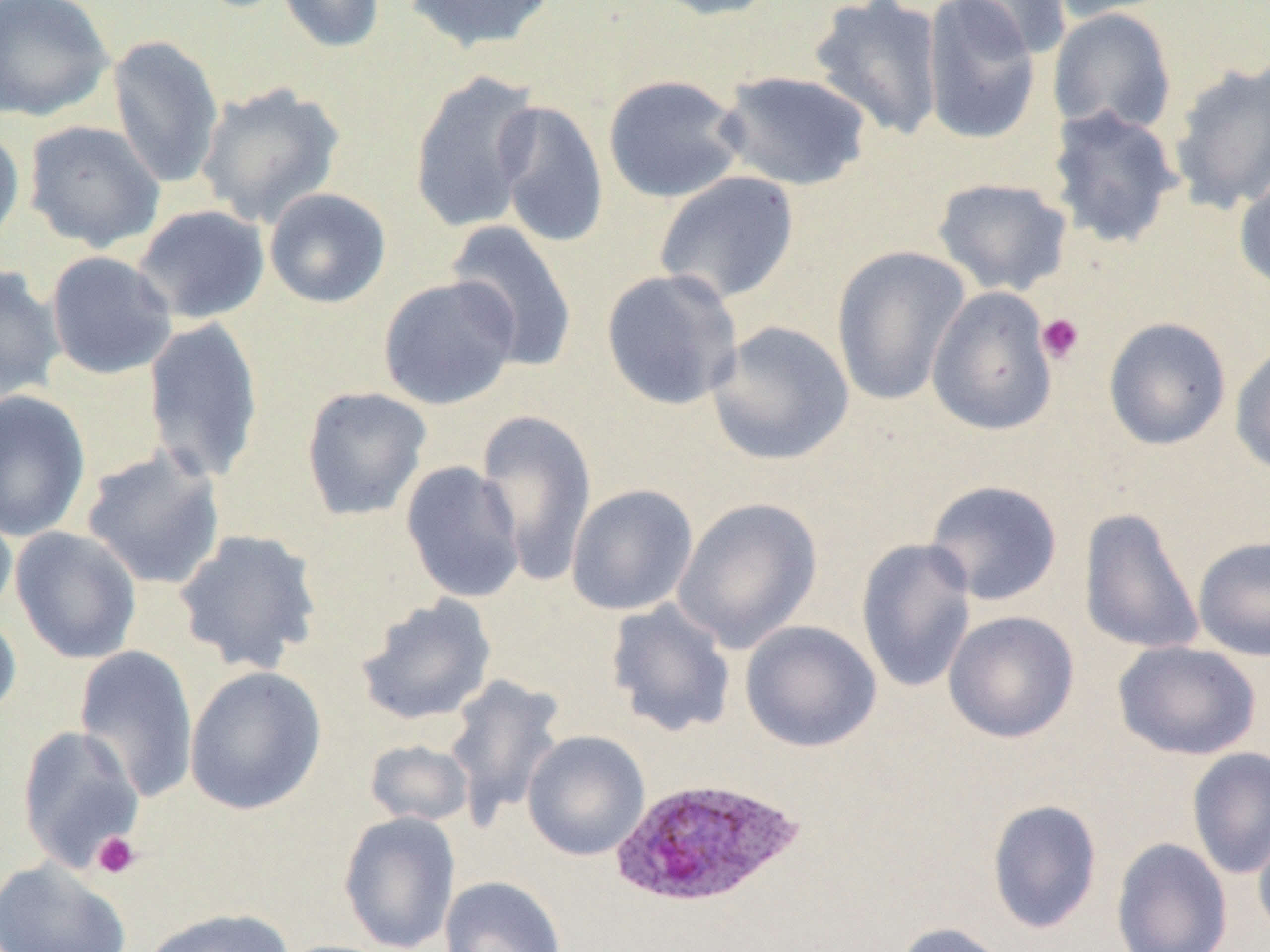

slide-level diagnosis = Plasmodium ovale
image size = 1270×952 pixels
preparation = thin blood film
modality = optical microscopy
field of view = one of a larger specimen
magnification = 1000x
uninfected red blood cell locations = approximate bounding boxes as [x1, y1, x2, y2] in pixels: [0, 0, 114, 122], [275, 0, 385, 54], [403, 0, 559, 52], [645, 0, 785, 21], [807, 0, 946, 141], [920, 0, 1043, 146], [946, 0, 1071, 60], [1041, 0, 1177, 23], [1047, 8, 1177, 137], [106, 34, 225, 190], [1167, 59, 1270, 217], [408, 70, 544, 233], [715, 70, 874, 192], [601, 74, 747, 204], [195, 82, 346, 228], [492, 100, 610, 250], [1045, 105, 1184, 249], [23, 120, 166, 252], [0, 126, 25, 254], [1234, 163, 1270, 294], [653, 171, 801, 307], [931, 177, 1074, 297], [264, 188, 392, 309], [132, 204, 270, 325], [445, 220, 579, 372], [831, 245, 972, 406], [45, 251, 178, 380], [0, 264, 64, 404], [600, 268, 744, 411], [378, 275, 521, 410], [926, 286, 1059, 437], [142, 317, 264, 484], [1103, 317, 1232, 451], [707, 320, 855, 466], [1230, 339, 1270, 477], [300, 386, 433, 521], [0, 389, 92, 542], [476, 409, 598, 586], [80, 446, 226, 590], [400, 461, 526, 603], [923, 479, 1063, 606], [565, 483, 698, 616], [672, 497, 823, 652], [0, 499, 18, 623], [1078, 506, 1206, 656], [10, 526, 142, 665], [173, 528, 323, 675], [1192, 536, 1270, 662], [855, 538, 977, 693], [355, 595, 498, 726], [605, 599, 737, 738], [0, 607, 21, 725], [943, 610, 1080, 743], [740, 620, 882, 753], [1113, 640, 1262, 760], [74, 643, 200, 804], [183, 665, 327, 816], [444, 673, 567, 830], [15, 725, 145, 873], [522, 730, 650, 861], [363, 739, 475, 827], [1186, 747, 1270, 880], [986, 799, 1103, 934], [338, 811, 461, 952], [1253, 818, 1270, 942], [1110, 837, 1233, 952], [0, 858, 132, 952], [439, 875, 567, 952], [138, 907, 294, 952], [892, 921, 1016, 952]
Plasmodium ovale-infected red blood cell locations = approximate bounding boxes as [x1, y1, x2, y2] in pixels: [608, 776, 805, 911]
platelet locations = approximate bounding boxes as [x1, y1, x2, y2] in pixels: [1037, 312, 1086, 365], [91, 831, 141, 879]